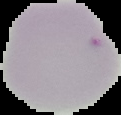

Cell region segmented out of the field of view; the surrounding area is masked to black. From a thin blood smear. Result: negative for Plasmodium parasites. Image is 121×115 pixels.